Identify the parasite.
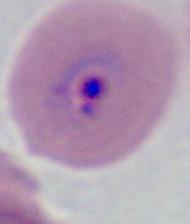
This is Plasmodium.

Micrograph. Captured at either 400x or 1000x magnification.